Locate every malaria parasite.
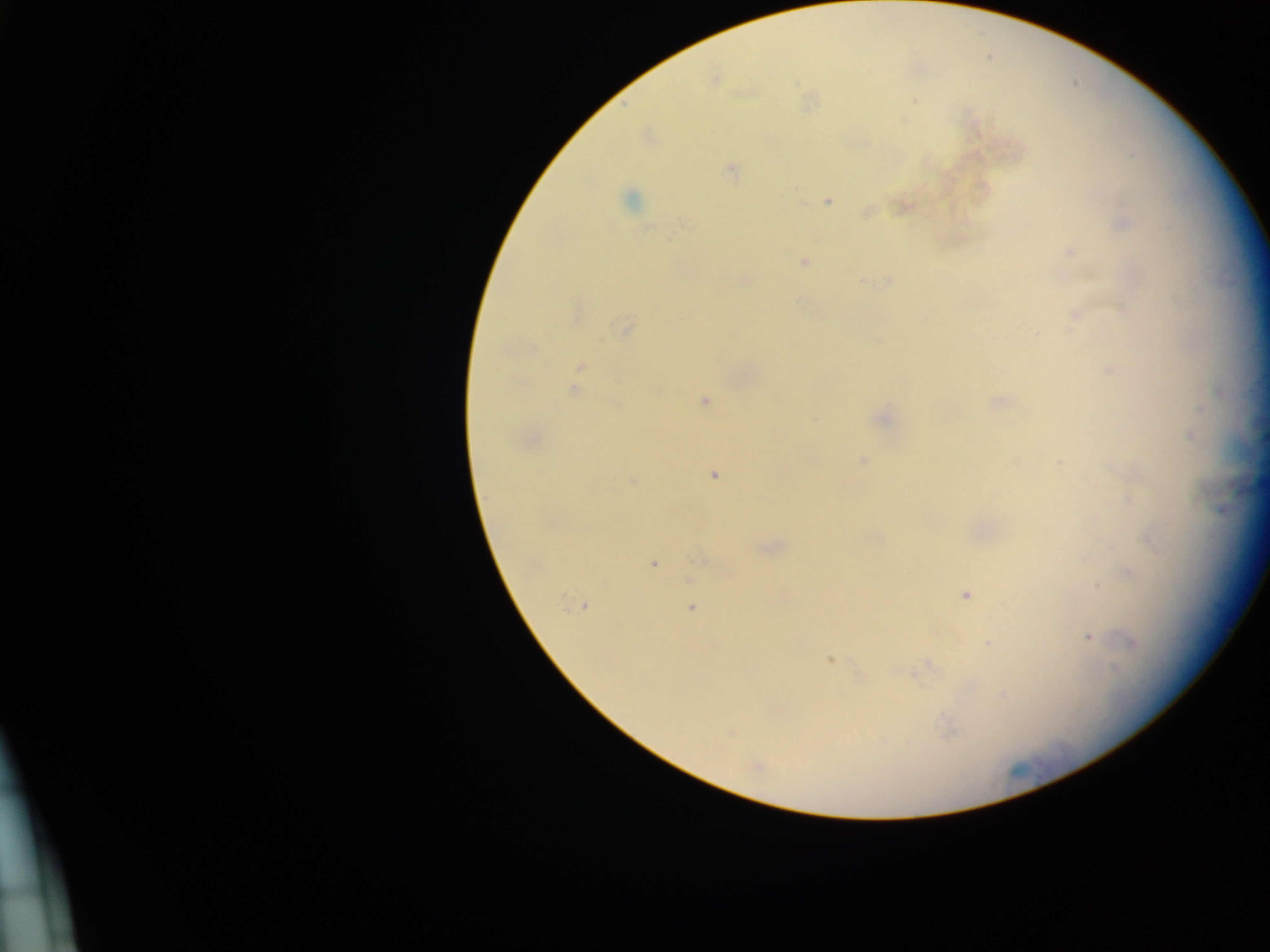

Approximate centers as (x, y) in pixels.
Malaria parasites: (807, 100), (914, 101), (865, 141), (1133, 155), (731, 170), (829, 200), (629, 201), (899, 206), (868, 211), (687, 223), (649, 227), (671, 236), (1073, 249), (803, 261), (1087, 272), (888, 279), (746, 280), (863, 282), (1077, 316), (622, 326), (880, 341), (1108, 369), (575, 388), (705, 401), (997, 402), (883, 413), (863, 459), (1057, 461), (712, 474), (632, 483), (1133, 496), (763, 547), (702, 558), (655, 564), (1131, 569), (1098, 586), (965, 594), (584, 606), (692, 609), (1089, 637), (988, 642), (831, 660), (927, 665), (951, 731), (733, 733).

{
  "capture": "mobile-phone photograph through a microscope",
  "preparation": "thick blood film",
  "country": "Ghana",
  "field_of_view": "single",
  "image_size": "1270×952 pixels"
}